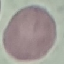
Result: no malaria parasites detected. Giemsa-stained preparation. Photographed with a smartphone camera at the microscope eyepiece. Thin smear of blood. Cell patch, automatically extracted from a larger field of view and resized to 64 × 64 pixels.